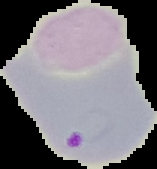
Summary:
  - Image size: 157×169 pixels
  - Image type: cell region segmented out of the field of view; surrounding area masked to black
  - Result: Plasmodium parasites identified
  - Preparation: thin blood smear